Locate every Plasmodium parasite.
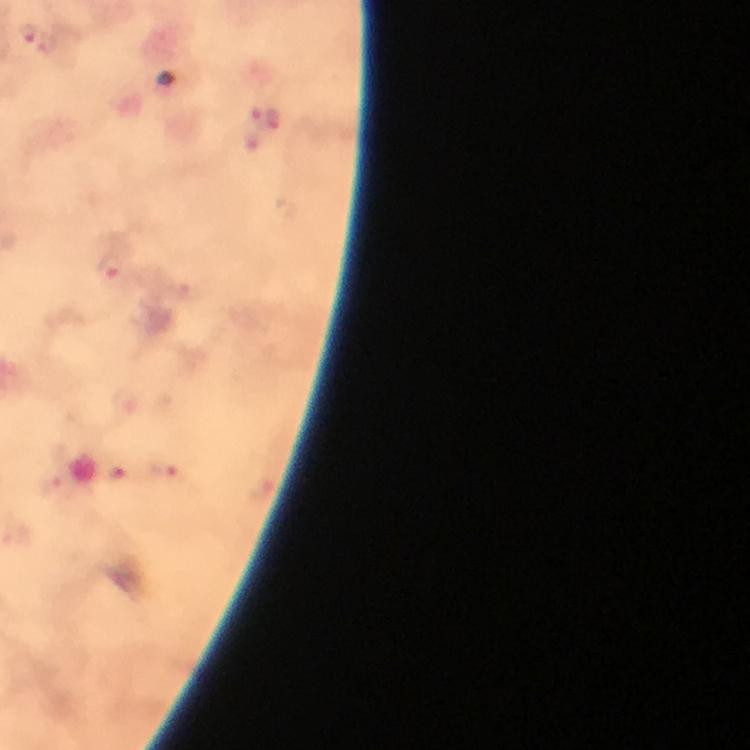
Approximate object centers, in pixels from the top-left corner.
Plasmodium parasites: (x=27, y=29), (x=255, y=118), (x=275, y=118), (x=110, y=267), (x=120, y=405), (x=166, y=472).

Immersion oil applied. Thick blood film. Giemsa stain. At 100x magnification. Image is 750×750 pixels. Cropped region of a single field of view. Photographed through the microscope with a smartphone camera. From a diagnostic examination for malaria.